Report the malaria status of this cell.
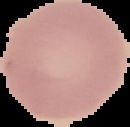
Uninfected.

image size = 130×127 pixels
image type = segmented cell region with the area outside set to black
preparation = thin blood film